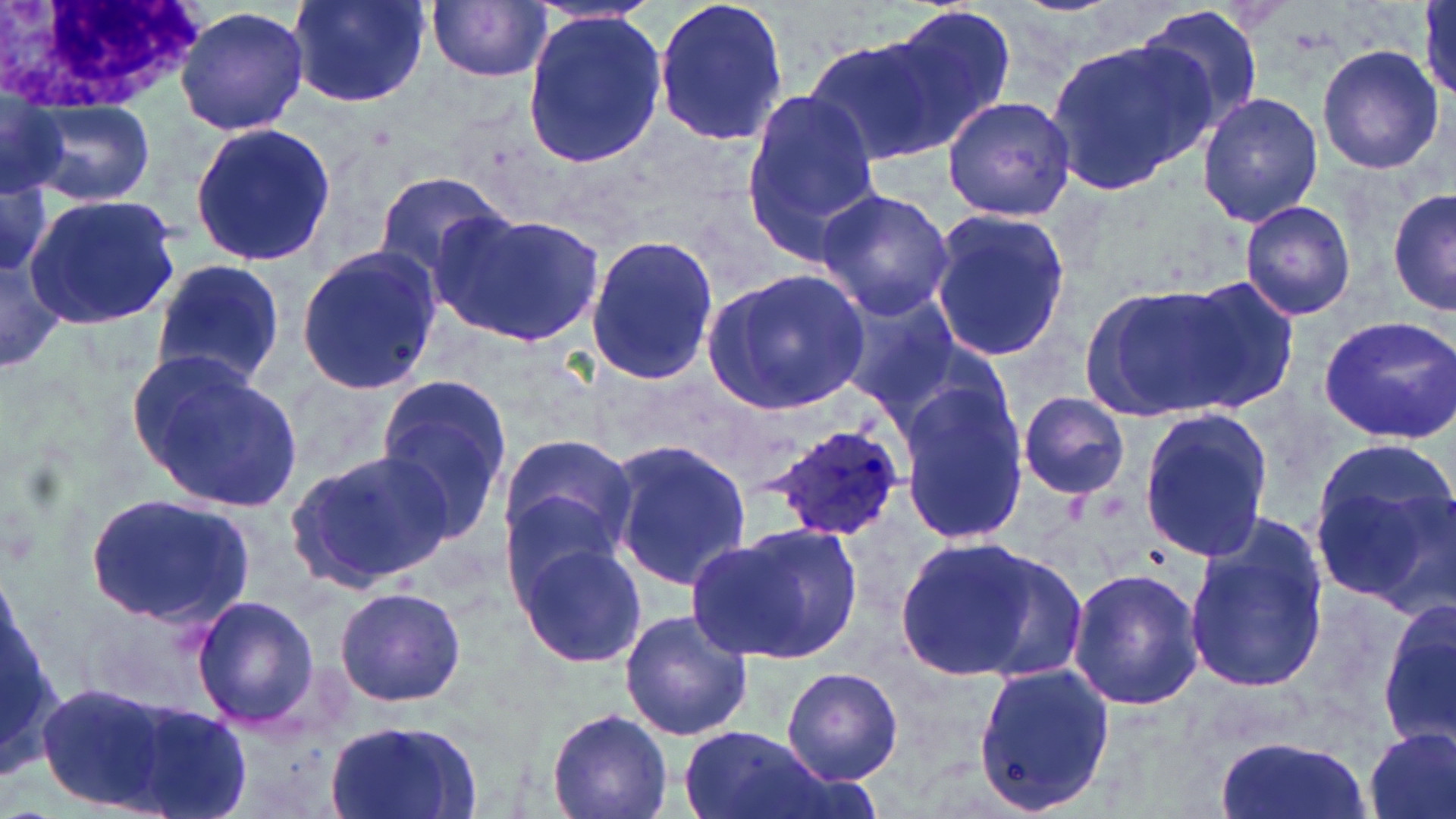

Summary:
  - Coordinate format: approximate bounding boxes as (x1,y1)-(x2,y2) corner pairs in pixels
  - Plasmodium ovale-infected red blood cell locations: (764,425)-(906,542)
  - White blood cell locations: (0,1)-(208,113)
  - Uninfected red blood cell locations: (287,0)-(430,111), (653,0)-(791,147), (427,1)-(553,84), (175,4)-(310,139), (1130,4)-(1267,139), (887,5)-(1018,142), (519,8)-(666,169), (802,30)-(955,166), (1045,35)-(1215,201), (1316,45)-(1444,175), (0,80)-(68,203), (740,90)-(883,258), (1196,92)-(1322,228), (942,94)-(1076,222), (26,98)-(155,205), (186,122)-(337,268), (0,171)-(53,275), (373,171)-(516,285), (1388,186)-(1455,317), (814,189)-(956,319), (24,192)-(182,328), (1239,200)-(1357,321), (431,207)-(608,350), (926,208)-(1070,365), (583,234)-(722,388), (295,243)-(444,396), (151,258)-(286,389), (704,269)-(869,414), (1177,276)-(1303,410), (1078,279)-(1247,424), (834,290)-(962,416), (1317,314)-(1456,444), (127,354)-(302,512), (374,373)-(514,535), (899,381)-(1029,546), (1019,392)-(1130,498), (1135,408)-(1277,565), (497,434)-(637,565), (609,438)-(751,591), (1305,445)-(1456,609), (285,447)-(457,592), (85,495)-(256,628), (1181,517)-(1327,697), (694,520)-(864,665), (888,534)-(1058,681), (511,536)-(648,671), (1067,567)-(1205,711), (335,585)-(466,707), (191,596)-(322,731), (1380,597)-(1456,753), (618,609)-(754,742), (971,661)-(1115,813), (782,667)-(903,784), (32,681)-(219,817), (125,708)-(253,819), (547,708)-(673,819), (322,719)-(485,819), (676,728)-(838,819), (1363,728)-(1455,819), (1212,731)-(1368,819)
  - Slide-level diagnosis: Plasmodium ovale
  - Field of view: single
  - Image size: 1456×819 pixels
  - Modality: optical microscopy
  - Preparation: thin blood smear
  - Stain: May-Grünwald-Giemsa
  - Magnification: 1000x